Name the cell type shown.
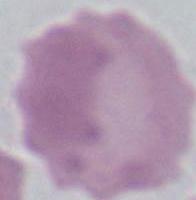

This is an erythrocyte.

Summary:
  - Modality: micrograph
  - Magnification: 1000x